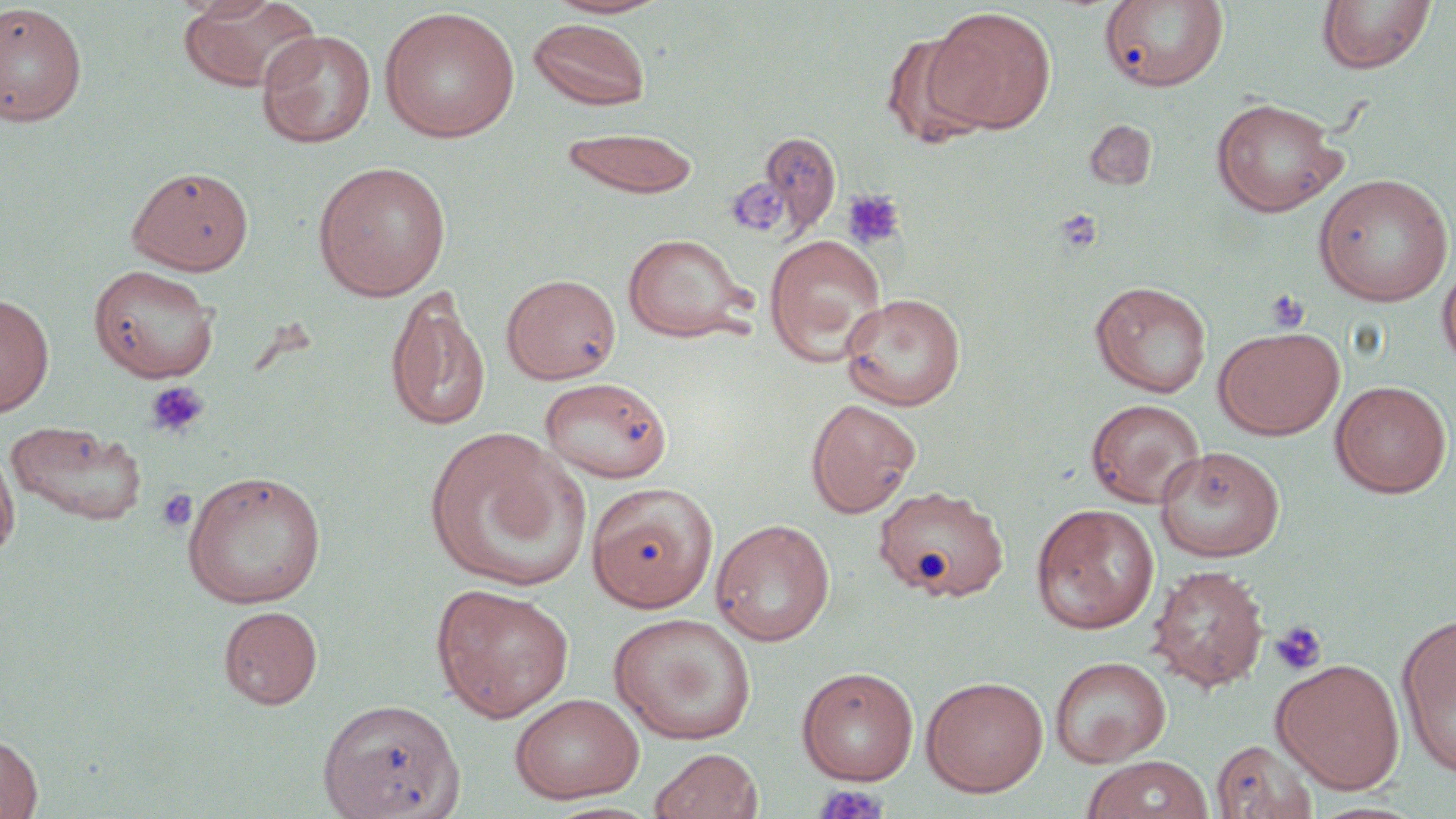 Approximate bounding boxes as named x1/y1/x2/y2 corners in pixels. Platelet locations: (x1=735, y1=182, x2=788, y2=239), (x1=842, y1=188, x2=905, y2=250), (x1=1055, y1=208, x2=1103, y2=254), (x1=1264, y1=288, x2=1310, y2=333), (x1=144, y1=380, x2=210, y2=439), (x1=156, y1=488, x2=198, y2=534), (x1=1269, y1=620, x2=1328, y2=675), (x1=813, y1=783, x2=890, y2=819). Uninfected red blood cell locations: (x1=177, y1=1, x2=321, y2=92), (x1=544, y1=1, x2=670, y2=19), (x1=1100, y1=1, x2=1230, y2=92), (x1=1316, y1=1, x2=1436, y2=74), (x1=0, y1=3, x2=88, y2=127), (x1=928, y1=6, x2=1057, y2=133), (x1=379, y1=7, x2=521, y2=143), (x1=527, y1=18, x2=652, y2=110), (x1=256, y1=29, x2=376, y2=148), (x1=882, y1=32, x2=995, y2=148), (x1=1210, y1=97, x2=1347, y2=217), (x1=1085, y1=119, x2=1157, y2=190), (x1=561, y1=127, x2=699, y2=199), (x1=757, y1=130, x2=842, y2=238), (x1=312, y1=161, x2=452, y2=301), (x1=127, y1=166, x2=254, y2=275), (x1=1313, y1=173, x2=1454, y2=307), (x1=622, y1=233, x2=754, y2=343), (x1=764, y1=234, x2=887, y2=365), (x1=1437, y1=259, x2=1456, y2=371), (x1=88, y1=263, x2=220, y2=382), (x1=501, y1=273, x2=621, y2=383), (x1=1090, y1=281, x2=1212, y2=398), (x1=385, y1=289, x2=490, y2=432), (x1=840, y1=292, x2=966, y2=410), (x1=0, y1=293, x2=54, y2=417), (x1=1213, y1=326, x2=1344, y2=440), (x1=539, y1=376, x2=672, y2=484), (x1=1330, y1=380, x2=1452, y2=498), (x1=806, y1=398, x2=921, y2=517), (x1=1085, y1=398, x2=1205, y2=508), (x1=6, y1=419, x2=148, y2=525), (x1=424, y1=428, x2=588, y2=592), (x1=0, y1=443, x2=19, y2=562), (x1=1154, y1=445, x2=1285, y2=562), (x1=180, y1=469, x2=327, y2=609), (x1=587, y1=482, x2=718, y2=611), (x1=873, y1=485, x2=1009, y2=601), (x1=1031, y1=503, x2=1159, y2=634), (x1=710, y1=518, x2=836, y2=646), (x1=1148, y1=564, x2=1269, y2=691), (x1=431, y1=583, x2=575, y2=721), (x1=218, y1=605, x2=323, y2=709), (x1=608, y1=612, x2=757, y2=745), (x1=1397, y1=613, x2=1456, y2=780), (x1=1050, y1=656, x2=1171, y2=767), (x1=1271, y1=658, x2=1405, y2=793), (x1=796, y1=666, x2=918, y2=785), (x1=921, y1=676, x2=1049, y2=797), (x1=509, y1=692, x2=644, y2=803), (x1=319, y1=697, x2=464, y2=819), (x1=0, y1=732, x2=43, y2=819), (x1=1211, y1=738, x2=1318, y2=819), (x1=650, y1=747, x2=763, y2=819), (x1=1081, y1=755, x2=1214, y2=819). Slide-level diagnosis: no evidence of blood parasites. Light microscopy. Captured at 1000x magnification. Thin blood smear. May-Grünwald-Giemsa-stained preparation. Image is 1456×819 pixels. One field of a larger specimen.